State which parasite is depicted.
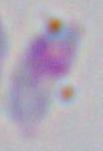
This is Toxoplasma gondii.

modality = photomicrograph
magnification = 1000x